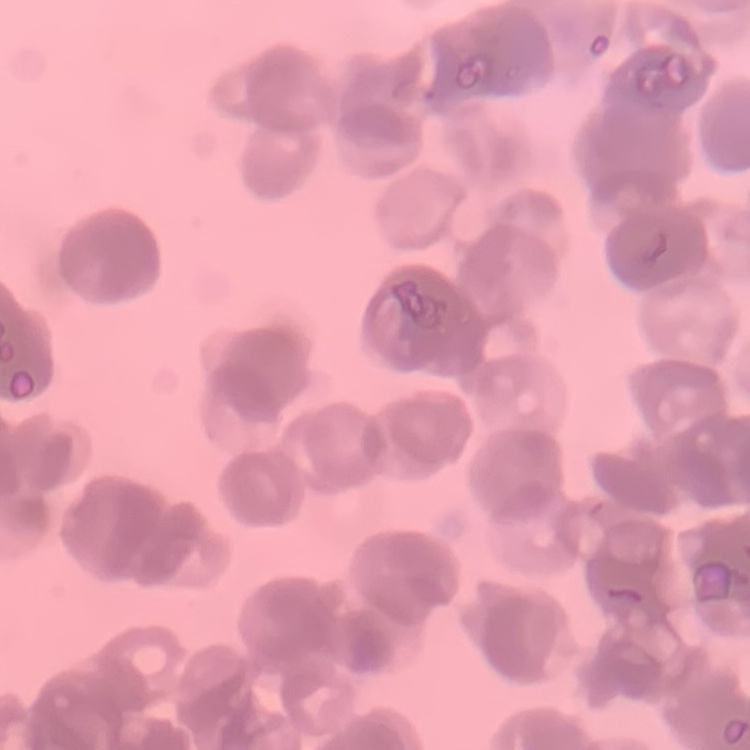
{
  "erythrocyte_morphology": "rouleaux formation",
  "image_type": "square crop of a larger photomicrograph",
  "preparation": "thin blood smear",
  "stain": "Field's or Giemsa"
}